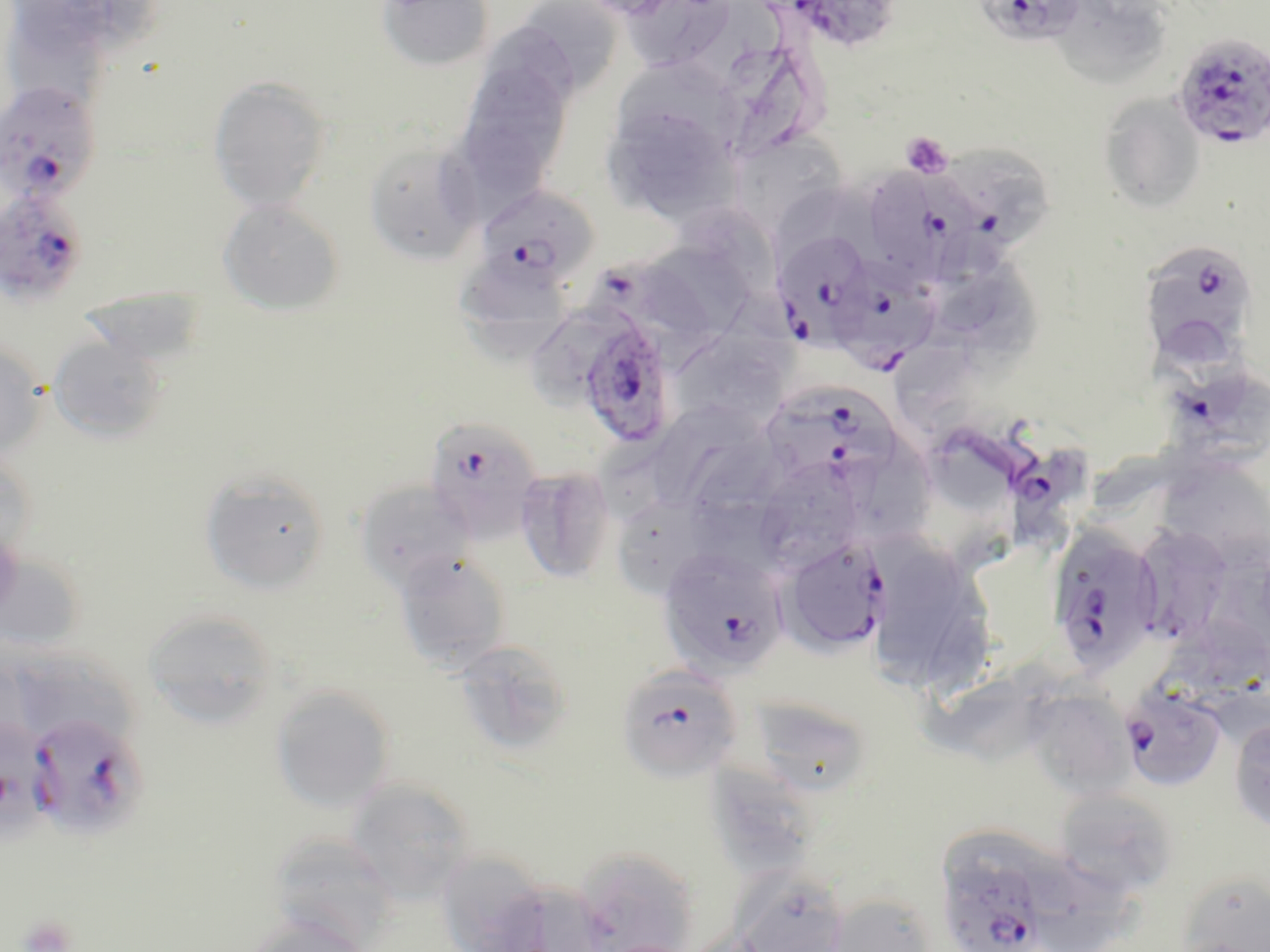 Approximate bounding boxes as (x1,y1)-(x2,y2) corner pairs in pixels. Uninfected red blood cell locations: (9,0)-(110,56), (376,0)-(494,72), (511,0)-(625,99), (687,0)-(783,82), (1059,0)-(1168,82), (614,1)-(741,73), (0,24)-(104,104), (723,51)-(815,160), (453,57)-(574,197), (616,61)-(746,141), (208,76)-(332,213), (1097,93)-(1207,215), (602,102)-(737,225), (729,132)-(849,235), (363,139)-(484,266), (778,186)-(879,248), (218,199)-(344,315), (676,202)-(780,291), (644,243)-(768,344), (942,257)-(1053,378), (459,260)-(568,357), (78,287)-(209,370), (672,334)-(789,428), (47,335)-(169,444), (0,339)-(47,460), (893,343)-(974,435), (924,395)-(1020,516), (658,407)-(768,510), (595,428)-(691,519), (850,436)-(933,555), (0,450)-(38,562), (763,459)-(862,573), (1168,462)-(1270,549), (514,466)-(617,584), (198,470)-(330,596), (353,479)-(474,593), (681,495)-(792,583), (618,502)-(704,590), (1129,522)-(1237,649), (0,549)-(88,656), (393,551)-(513,674), (875,552)-(959,690), (142,608)-(281,729), (1159,617)-(1270,700), (452,638)-(575,757), (29,641)-(141,739), (924,662)-(1084,763), (270,683)-(396,813), (1024,687)-(1137,800), (747,694)-(874,799), (1228,715)-(1270,833), (710,759)-(817,895), (346,778)-(476,902), (1052,787)-(1180,898), (941,828)-(1071,909), (266,835)-(401,949), (573,847)-(700,952), (451,851)-(543,952), (1041,859)-(1147,951), (732,870)-(850,952), (1178,872)-(1270,951), (484,879)-(611,952), (827,893)-(938,952), (241,913)-(372,952). Plasmodium falciparum-infected red blood cell locations: (775,0)-(903,53), (973,0)-(1089,49), (1172,34)-(1270,150), (0,82)-(102,206), (922,144)-(1058,258), (869,168)-(988,280), (473,184)-(600,294), (0,187)-(92,309), (771,229)-(875,343), (1137,240)-(1258,365), (825,255)-(941,369), (589,264)-(719,364), (571,310)-(676,449), (1151,322)-(1254,431), (767,381)-(901,486), (423,415)-(545,543), (1005,444)-(1102,547), (1044,525)-(1165,673), (780,536)-(889,654), (658,545)-(789,677), (615,662)-(743,783), (1117,684)-(1228,793), (23,710)-(150,840), (935,870)-(1054,952). Platelet locations: (901,131)-(953,178), (16,914)-(78,952). Slide-level diagnosis: Plasmodium falciparum. Optical microscopy. 1000x magnification. Image is 1270×952 pixels. One field of a larger specimen. Thin blood film. May-Grünwald-Giemsa stain.